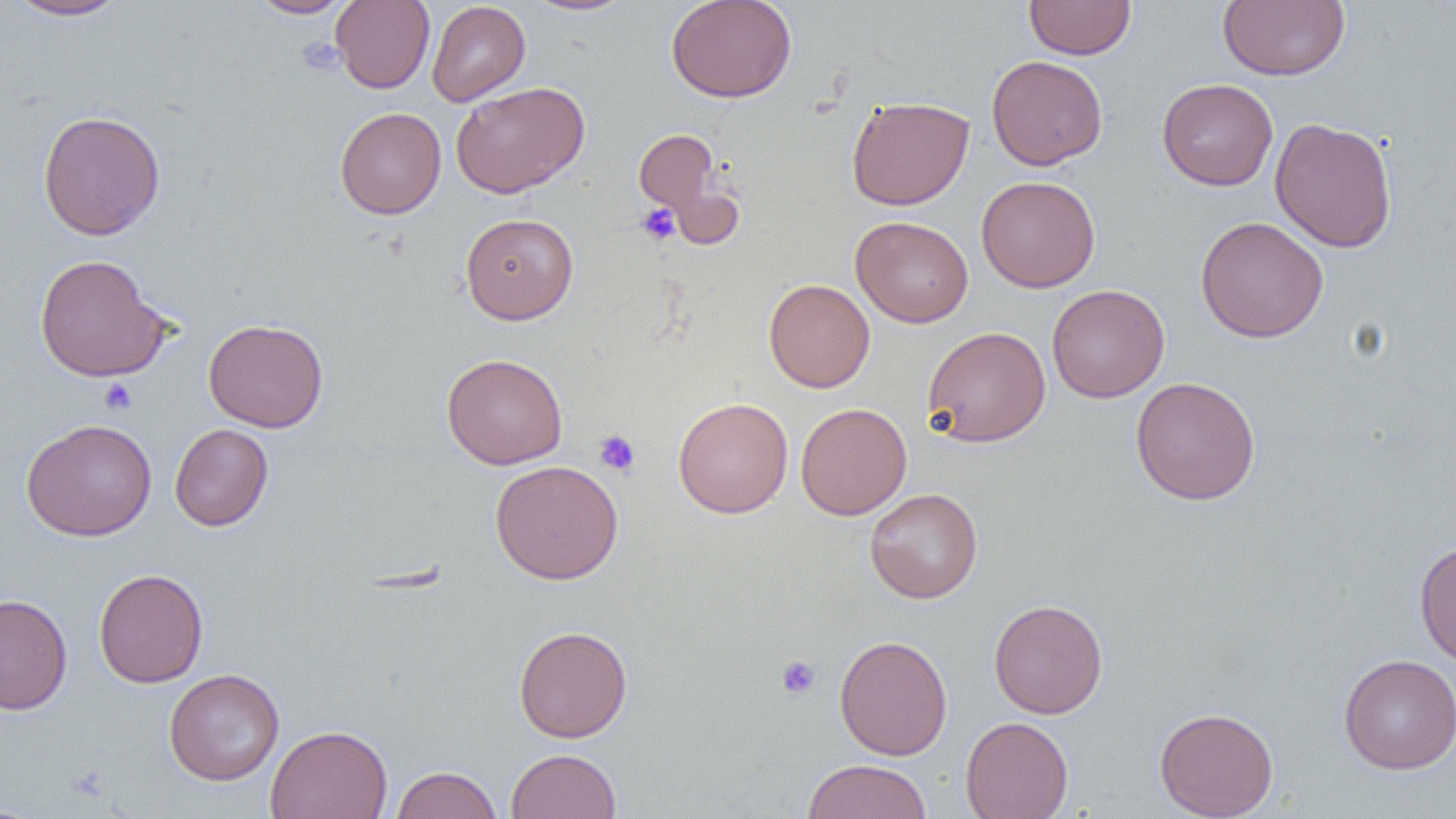 Approximate bounding boxes as (x1, y1, x2, y2) in pixels. Uninfected red blood cell locations: (5, 0, 129, 21), (248, 0, 354, 19), (330, 0, 435, 93), (522, 0, 637, 16), (666, 0, 797, 103), (1217, 0, 1350, 81), (426, 1, 530, 106), (1024, 1, 1136, 60), (986, 55, 1108, 170), (1157, 78, 1278, 190), (451, 81, 590, 198), (846, 95, 974, 210), (334, 107, 446, 219), (37, 110, 166, 240), (1269, 117, 1397, 253), (633, 128, 721, 218), (976, 175, 1100, 293), (460, 213, 579, 324), (850, 216, 974, 328), (1195, 216, 1329, 343), (33, 254, 171, 382), (763, 279, 875, 393), (1046, 284, 1169, 403), (203, 318, 329, 432), (922, 325, 1051, 447), (441, 353, 568, 469), (1131, 376, 1261, 505), (672, 397, 794, 518), (795, 403, 911, 520), (21, 418, 157, 541), (169, 423, 274, 531), (490, 460, 623, 584), (865, 487, 983, 604), (1414, 541, 1456, 670), (93, 568, 209, 688), (0, 593, 73, 715), (988, 598, 1108, 718), (513, 624, 632, 742), (834, 634, 953, 760), (1338, 653, 1456, 774), (164, 668, 285, 785), (1154, 707, 1279, 818), (960, 716, 1073, 819), (265, 724, 393, 819), (505, 748, 622, 818), (800, 759, 932, 819), (389, 765, 503, 819), (0, 802, 48, 818). Platelet locations: (296, 37, 345, 75), (636, 203, 681, 246), (98, 378, 138, 415), (593, 429, 641, 477), (776, 655, 821, 699). Slide-level diagnosis: negative for blood parasites. Light microscopy. Image is 1456×819 pixels. Captured at 1000x magnification. Single field of view. Thin blood smear.